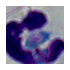
Photomicrograph. A leukocyte is shown. Captured at 1000x magnification.